Identify the parasite.
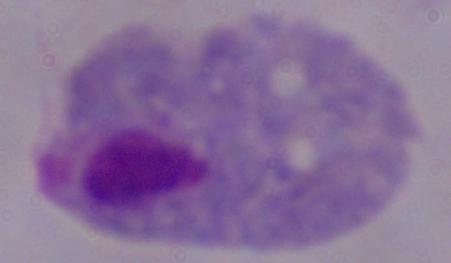
This is a trichomonad.

Captured at 1000x magnification. Micrograph.